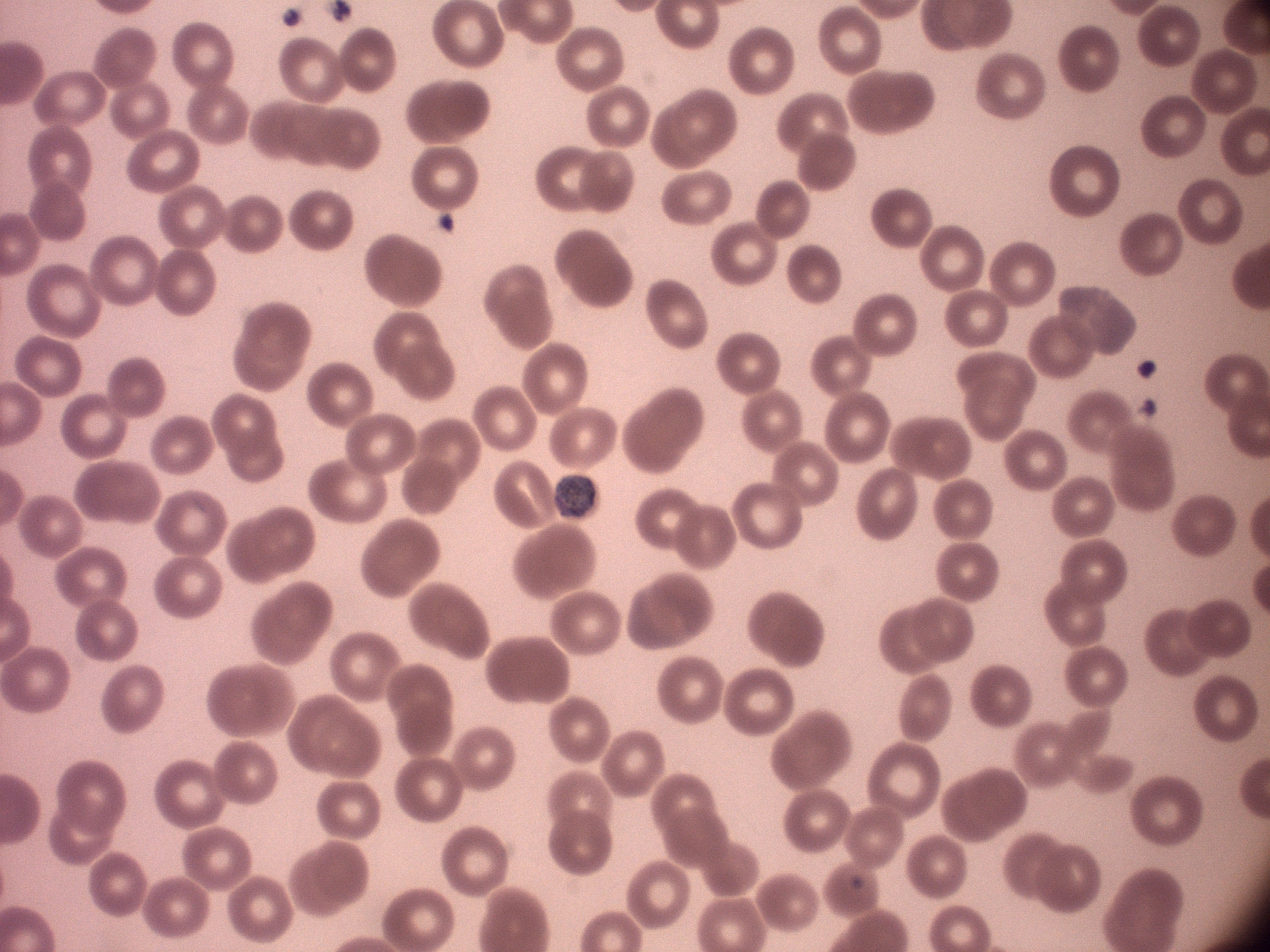

Approximate bounding boxes as named x1/y1/x2/y2 corners in pixels, from the source annotation, which is not necessarily exhaustive.
Summary:
  - Gametocyte locations: (x1=554, y1=475, x2=595, y2=517)
  - Stain: Giemsa
  - Preparation: thin blood smear
  - Microscope: Leica DM2000 with built-in camera
  - Image size: 1270×952 pixels
  - Species: Plasmodium malariae
  - Field of view: single
  - Magnification: 100x